Outline each P. falciparum parasite and classify it by life-cycle stage.
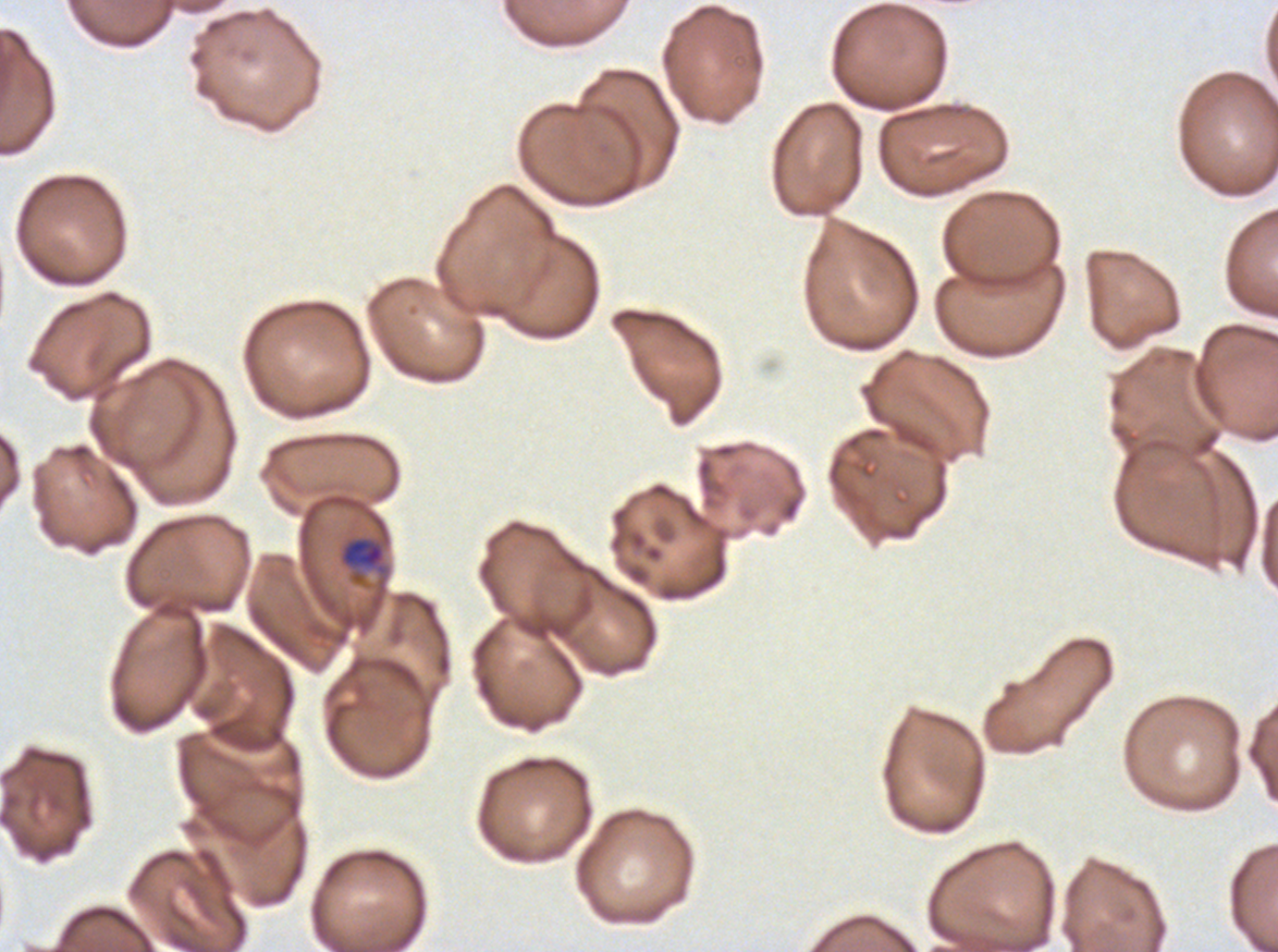

Approximate bounding rectangles given as corner coordinates in pixels from the top-left.
Late-ring/early-trophozoite forms: (x1=338, y1=535, x2=388, y2=585).
No rings, mid trophozoites, late trophozoites, early schizonts, late schizonts, segmenters, or gametocytes observed.

Summary:
  - Preparation: thin blood smear
  - Field of view: one sub-image of a larger composite
  - Specimen: ex-vivo P. falciparum culture from a patient in The Gambia, grown for 24 to 48 hours
  - Image size: 1278×952 pixels
  - Stain: Giemsa